State which cell type is depicted.
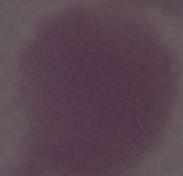
An erythrocyte.

magnification = 1000x
modality = micrograph